Locate every Plasmodium vivax-infected red blood cell.
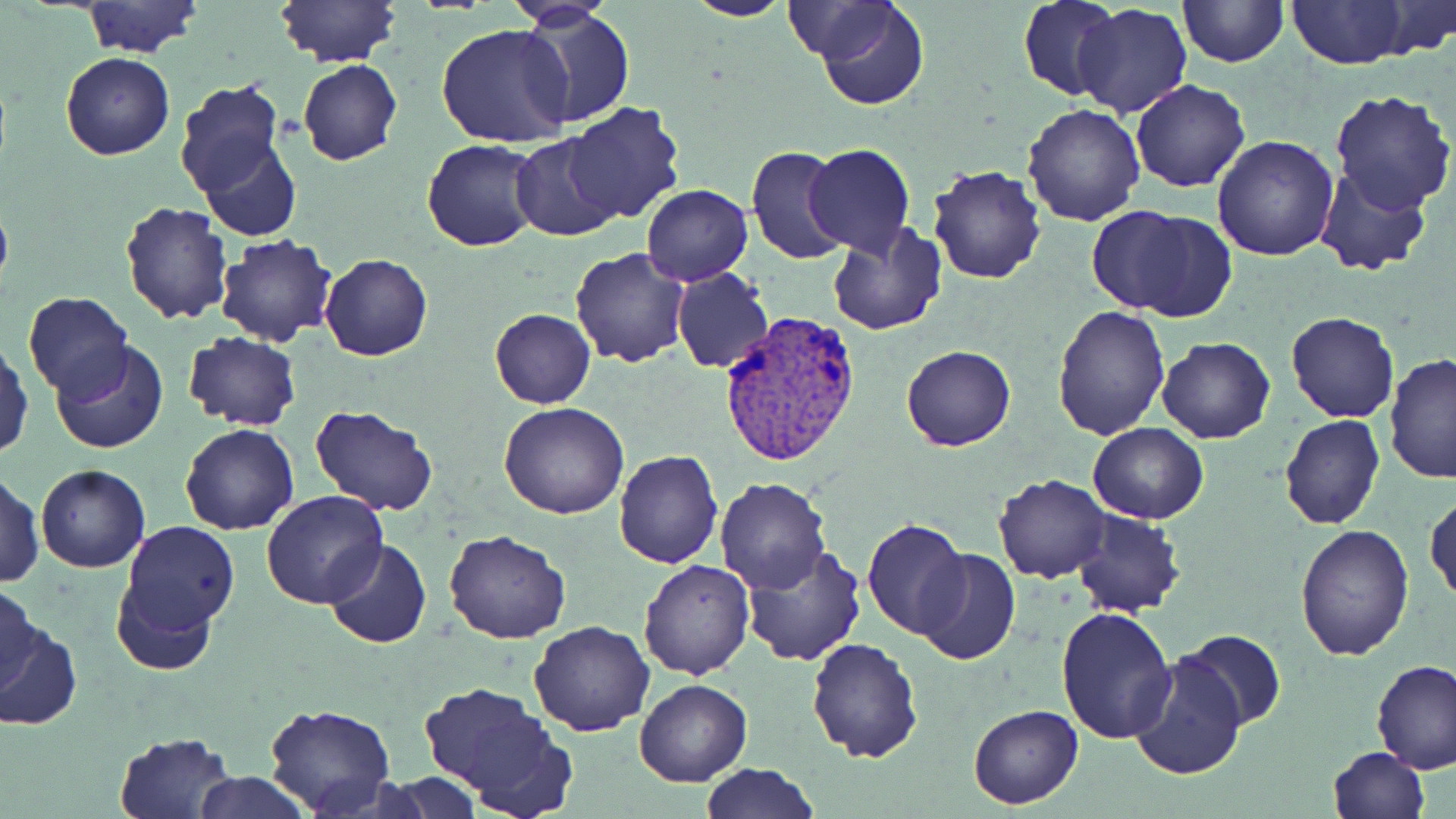
Approximate bounding boxes as (x1, y1, x2, y2) in pixels.
Plasmodium vivax-infected red blood cells: (720, 311, 863, 468).

Summary:
  - Uninfected red blood cell locations: (275, 0, 400, 68), (683, 0, 794, 23), (814, 0, 928, 110), (1285, 0, 1413, 69), (1377, 0, 1456, 58), (502, 1, 621, 28), (1017, 1, 1122, 102), (1179, 1, 1286, 67), (82, 2, 202, 56), (1073, 4, 1193, 119), (516, 9, 636, 128), (435, 24, 574, 150), (1086, 39, 1212, 164), (61, 53, 175, 159), (298, 59, 402, 166), (171, 78, 289, 201), (1131, 78, 1250, 193), (1329, 87, 1456, 213), (563, 102, 688, 224), (1022, 103, 1148, 226), (1212, 134, 1340, 260), (197, 135, 303, 241), (511, 135, 623, 242), (423, 139, 546, 253), (803, 144, 915, 257), (746, 145, 850, 266), (928, 164, 1047, 284), (1313, 166, 1433, 278), (641, 183, 754, 286), (0, 195, 13, 300), (121, 201, 232, 325), (1085, 204, 1230, 320), (827, 224, 949, 336), (215, 232, 340, 348), (569, 247, 691, 367), (320, 253, 433, 361), (672, 267, 774, 372), (22, 291, 133, 401), (1052, 304, 1170, 441), (491, 309, 595, 409), (1286, 311, 1397, 422), (183, 330, 302, 430), (1155, 337, 1276, 443), (0, 339, 33, 459), (51, 341, 168, 455), (901, 345, 1016, 450), (1384, 353, 1456, 486), (499, 401, 629, 519), (310, 404, 439, 515), (1279, 413, 1385, 530), (1087, 422, 1210, 524), (180, 423, 299, 535), (614, 449, 723, 569), (35, 465, 149, 572), (1, 471, 44, 588), (993, 474, 1111, 582), (714, 476, 830, 593), (260, 492, 387, 610), (1426, 493, 1456, 607), (1072, 509, 1185, 618), (114, 519, 240, 649), (861, 519, 970, 638), (1294, 523, 1416, 661), (442, 531, 568, 645), (324, 539, 431, 650), (741, 543, 868, 666), (915, 548, 1021, 666), (639, 556, 754, 678), (0, 581, 42, 695), (1055, 605, 1178, 743), (529, 619, 655, 737), (0, 624, 81, 731), (1180, 631, 1286, 729), (806, 636, 924, 761), (1128, 653, 1248, 780), (1371, 658, 1456, 773), (634, 679, 752, 787), (418, 680, 569, 810), (263, 702, 396, 818), (968, 704, 1083, 808), (112, 732, 238, 819), (1328, 746, 1429, 817), (700, 761, 820, 819), (193, 772, 310, 818), (384, 774, 484, 818)
  - Slide-level diagnosis: Plasmodium vivax
  - Field of view: single
  - Stain: May-Grünwald-Giemsa
  - Image size: 1456×819 pixels
  - Magnification: 1000x
  - Modality: optical microscopy
  - Preparation: thin blood smear